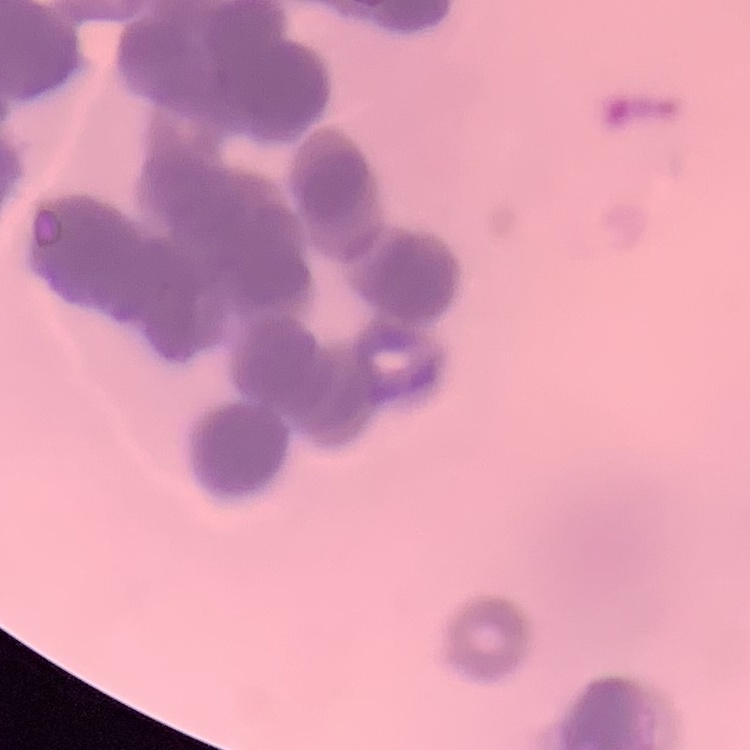

The red blood cells exhibit rouleaux formation. Square crop of a larger photomicrograph. Field's or Giemsa stain. Thin blood film.